Classify this cell by malaria status.
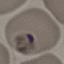
Uninfected.

{
  "image_type": "cell patch, automatically extracted from a larger field of view and resized to 64 × 64 pixels",
  "stain": "Giemsa",
  "preparation": "thin blood smear",
  "capture": "smartphone through the microscope eyepiece"
}